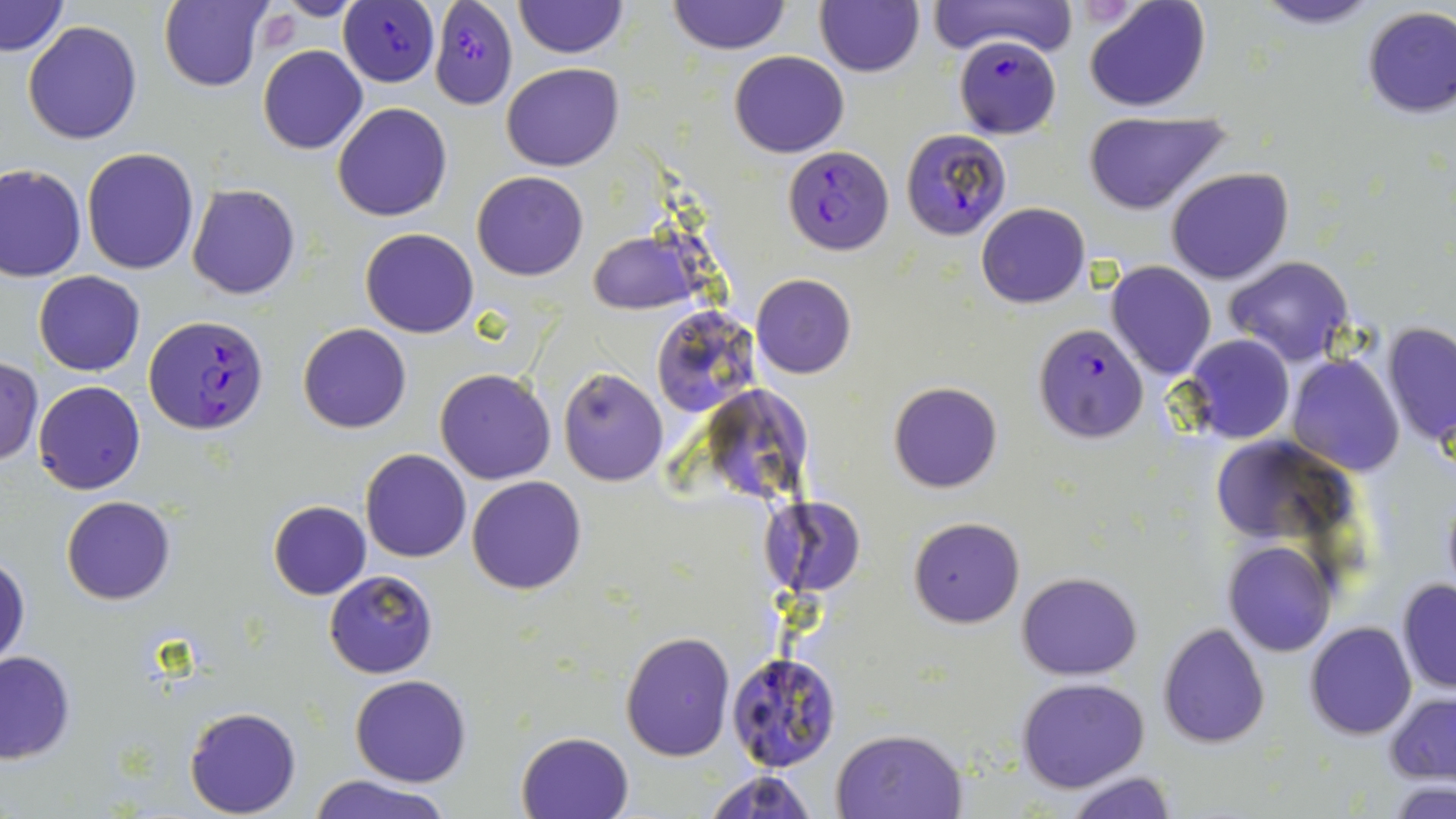

slide_level_diagnosis: Plasmodium falciparum
preparation: thin blood film
field_of_view: single
plasmodium_falciparum_infected_red_blood_cell_locations: 'approximate bounding boxes as (x1, y1, x2, y2) in pixels: (337, 0, 444, 86), (429, 0, 517, 107), (954, 35, 1060, 140), (899, 128, 1012, 241), (783, 146, 894, 257), (144, 315, 270, 435), (1032, 323, 1149, 442)'
modality: light microscopy
image_size: 1456×819 pixels
uninfected_red_blood_cell_locations: 'approximate bounding boxes as (x1, y1, x2, y2) in pixels: (159, 0, 273, 92), (268, 0, 367, 21), (814, 0, 924, 77), (927, 0, 1077, 57), (1084, 0, 1212, 113), (1250, 0, 1386, 30), (1, 1, 70, 57), (513, 1, 626, 59), (666, 1, 790, 54), (1359, 6, 1455, 119), (22, 21, 144, 145), (258, 45, 367, 155), (730, 51, 849, 157), (501, 63, 624, 171), (333, 101, 454, 221), (1082, 111, 1231, 215), (81, 147, 200, 275), (0, 163, 86, 282), (1166, 166, 1293, 284), (471, 171, 589, 281), (187, 184, 302, 299), (976, 202, 1089, 309), (360, 227, 479, 339), (586, 229, 702, 314), (1224, 257, 1353, 368), (1106, 262, 1217, 380), (33, 270, 146, 376), (752, 273, 856, 379), (652, 306, 759, 416), (1382, 321, 1456, 450), (299, 323, 412, 433), (1182, 334, 1296, 445), (1285, 354, 1405, 476), (0, 357, 44, 465), (558, 367, 668, 486), (434, 368, 557, 485), (32, 381, 146, 495), (889, 382, 1002, 493), (1207, 436, 1367, 565), (360, 449, 471, 562), (467, 475, 587, 595), (1437, 480, 1456, 602), (762, 494, 867, 598), (61, 496, 177, 605), (268, 501, 371, 600), (908, 517, 1025, 628), (1221, 539, 1337, 657), (1, 552, 30, 670), (323, 570, 438, 678), (1017, 572, 1141, 678), (1396, 578, 1456, 693), (1305, 622, 1416, 739), (1157, 624, 1270, 748), (620, 631, 735, 761), (0, 651, 76, 764), (727, 651, 843, 774), (350, 673, 472, 786), (1017, 678, 1148, 792), (1383, 693, 1455, 784), (185, 705, 302, 817), (830, 727, 968, 818), (516, 731, 634, 819), (702, 767, 819, 819), (1064, 770, 1180, 819), (310, 775, 453, 819), (1388, 779, 1456, 818)'
magnification: 1000x
stain: May-Grünwald-Giemsa